State the preparation type.
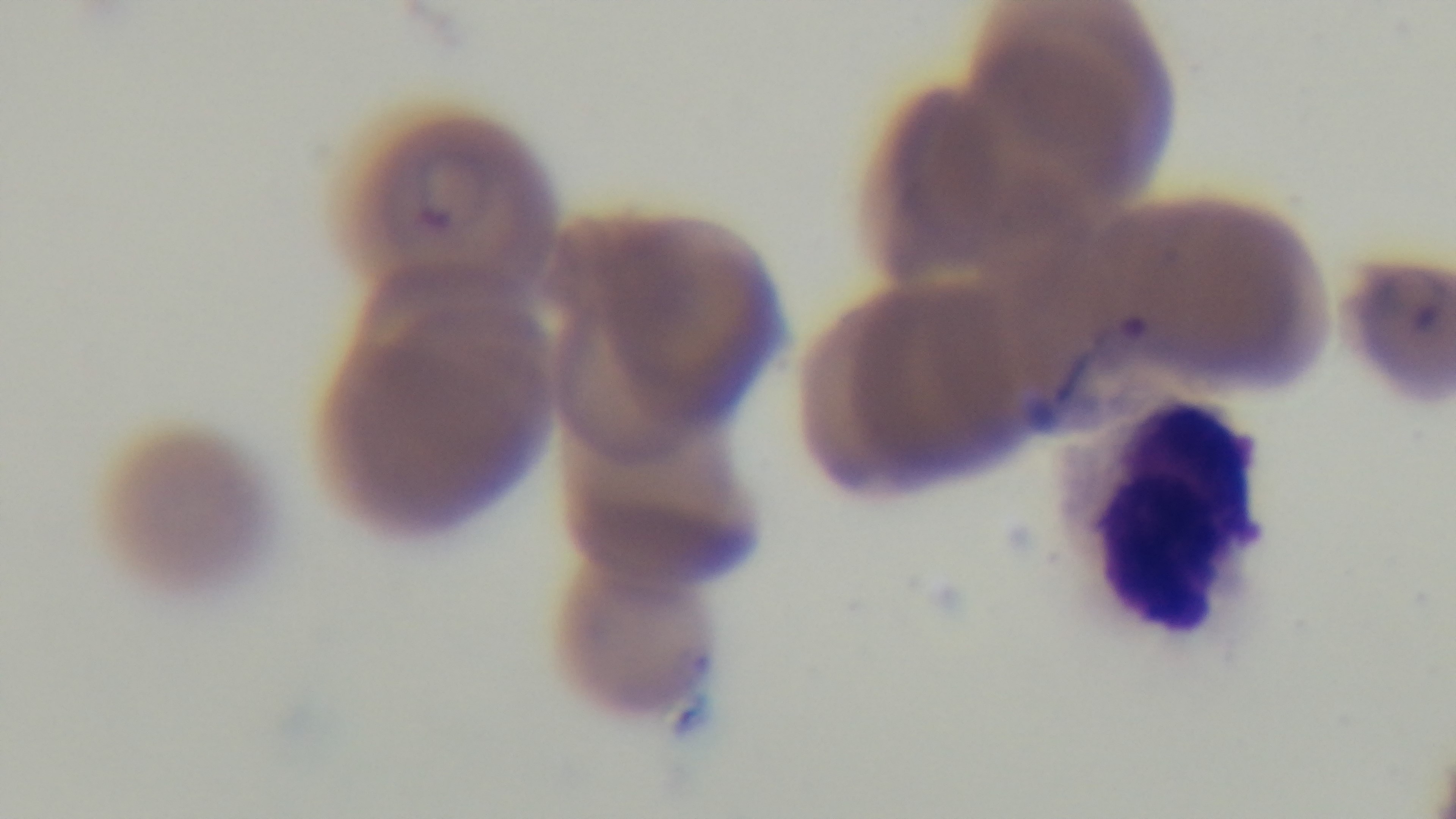

It is a thin blood film.

Summary:
  - Objective: 100x oil immersion
  - Malaria status: infected
  - Field of view: one from the slide
  - Capture: mounted 4K digital camera
  - Stain: Giemsa
  - Modality: light microscopy